Locate every leukocyte (white blood cell).
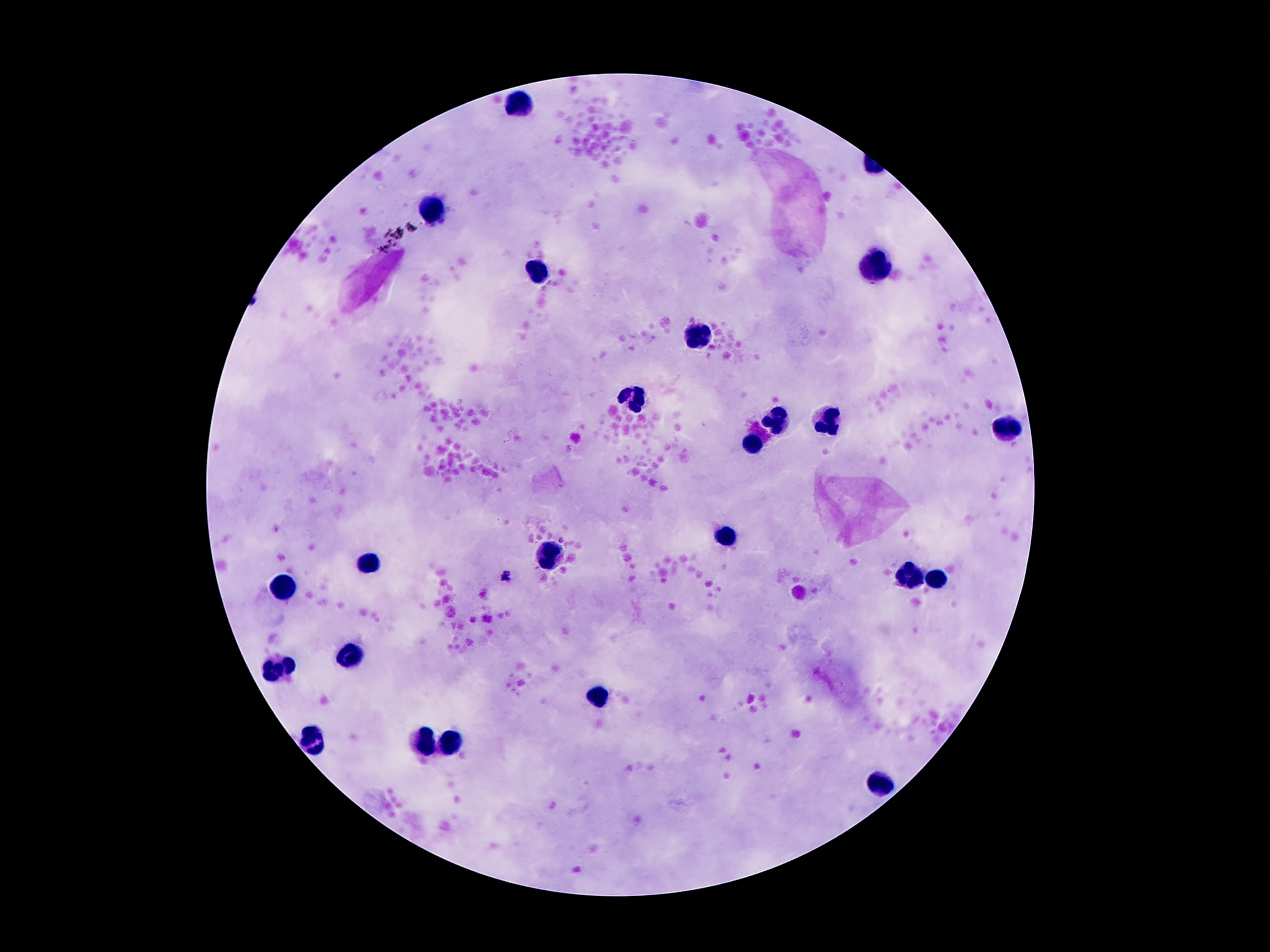
Approximate centers as [x, y] in pixels.
Leukocytes: [517, 102], [437, 210], [873, 264], [543, 273], [701, 335], [632, 399], [830, 420], [777, 422], [1010, 426], [750, 442], [724, 538], [552, 555], [371, 562], [904, 576], [937, 580], [283, 587], [353, 656], [283, 668], [599, 693], [314, 740], [423, 742], [455, 742], [881, 787].

capture = smartphone camera through the microscope eyepiece
stain = Giemsa
field of view = single
preparation = thick blood smear
image size = 1270×952 pixels
magnification = 100x
patient malaria status = uninfected